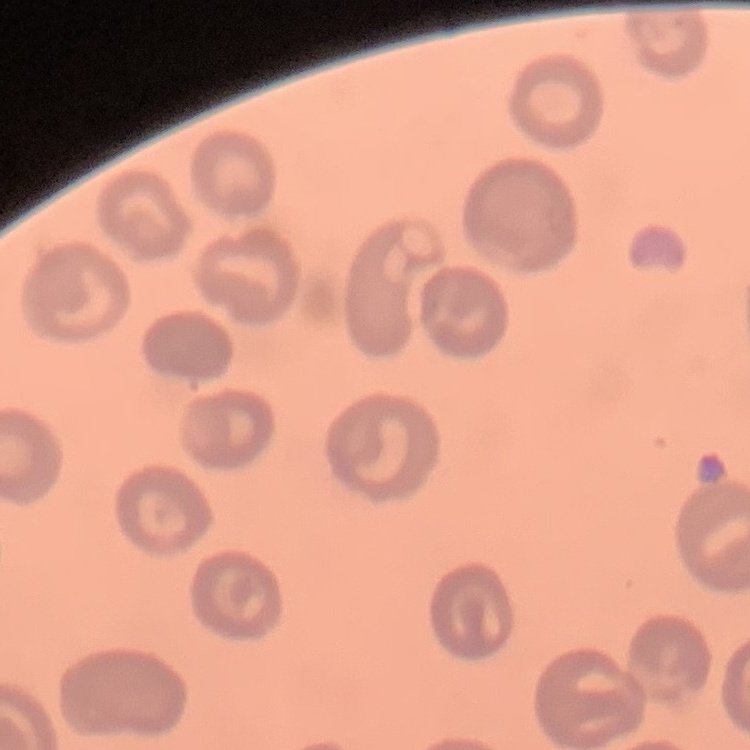
Summary:
  - Erythrocyte morphology: no rouleaux formation
  - Image type: one tile cut from a larger photomicrograph
  - Stain: Field's or Giemsa
  - Preparation: thin blood film